State which parasite is depicted.
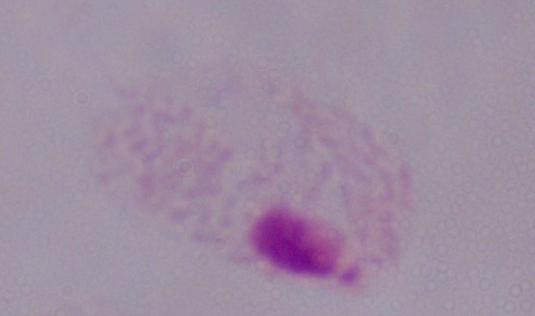

A trichomonad.

modality = photomicrograph
magnification = 1000x